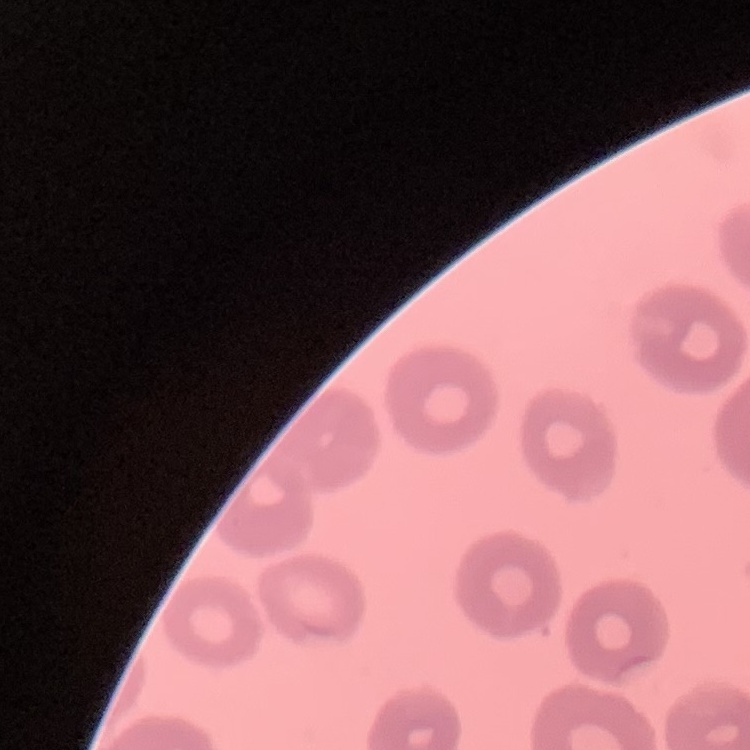

erythrocyte morphology = no rouleaux formation
image type = one tile cut from a larger photomicrograph
stain = Field's or Giemsa
preparation = thin peripheral smear